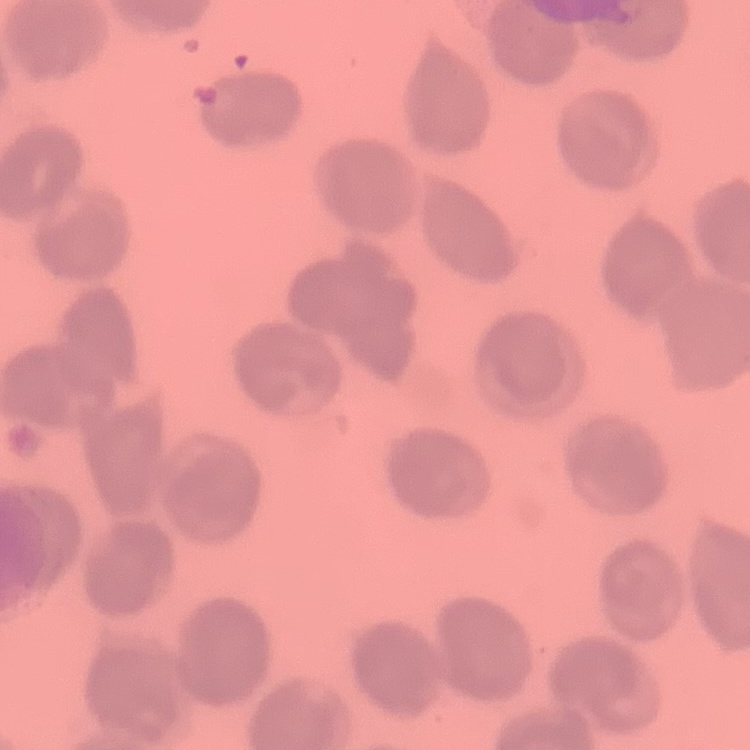

erythrocyte_morphology: no rouleaux formation
image_type: one tile cut from a larger photomicrograph
stain: Field's or Giemsa
preparation: thin blood film